Assess this cell for malaria.
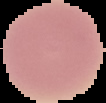
It is uninfected.

{
  "image_type": "cell region segmented out of the field of view; surrounding area masked to black",
  "preparation": "thin blood smear",
  "image_size": "106×103 pixels"
}